Locate every Plasmodium falciparum-infected red blood cell.
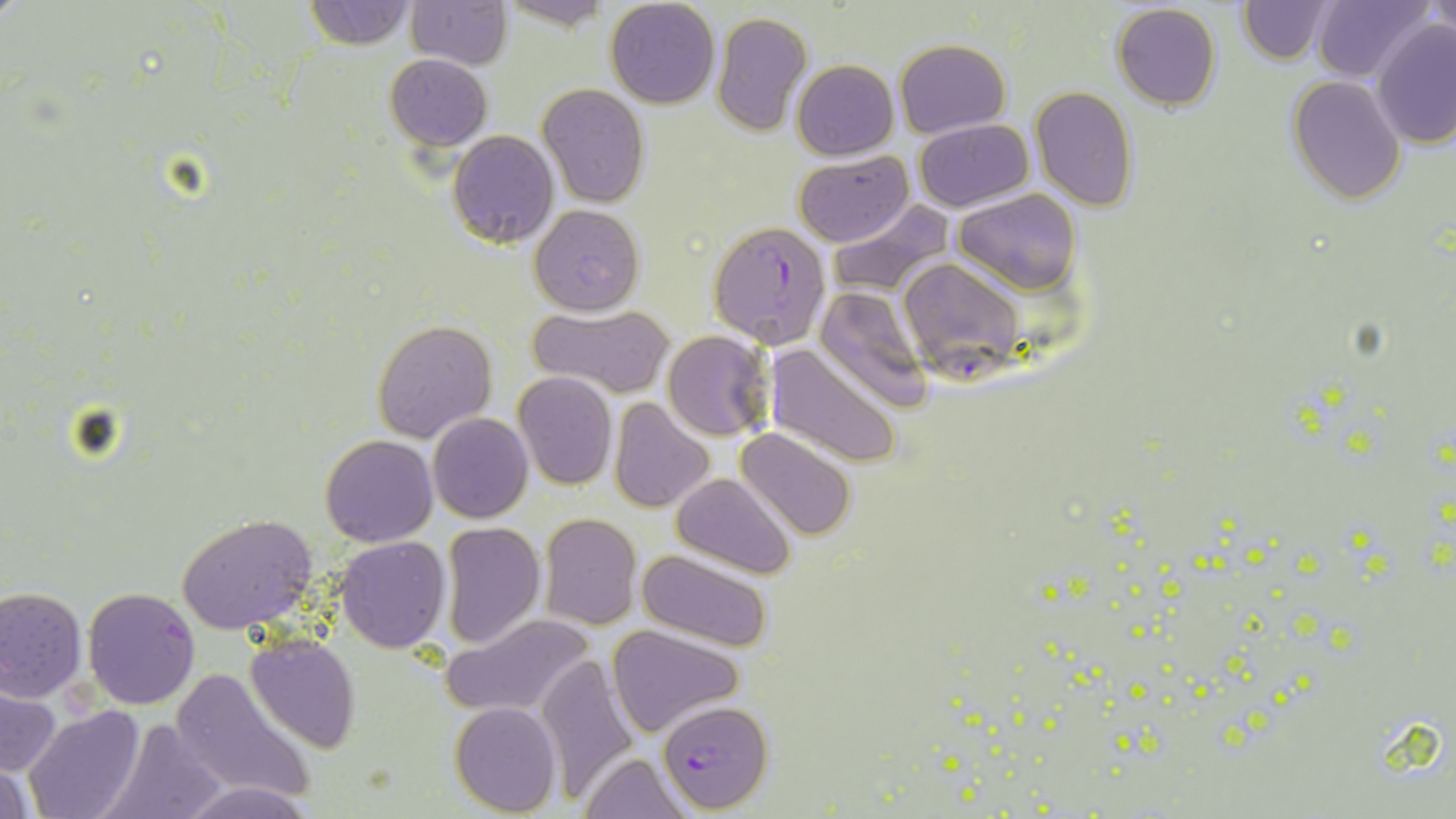
Approximate bounding boxes as [x1, y1, x2, y2] in pixels.
Plasmodium falciparum-infected red blood cells: [707, 220, 834, 349], [897, 257, 1028, 381], [658, 698, 771, 811].

slide-level diagnosis = Plasmodium falciparum
image size = 1456×819 pixels
stain = May-Grünwald-Giemsa
preparation = thin blood smear
field of view = one of a larger specimen
uninfected red blood cell locations = approximate bounding boxes as [x1, y1, x2, y2] in pixels: [304, 0, 415, 48], [406, 0, 512, 68], [606, 0, 719, 109], [1237, 0, 1331, 64], [1425, 0, 1455, 38], [1311, 1, 1430, 82], [494, 3, 617, 32], [1112, 5, 1221, 111], [711, 11, 812, 137], [1371, 19, 1456, 150], [894, 38, 1011, 137], [385, 54, 491, 149], [791, 59, 899, 160], [1288, 75, 1406, 205], [538, 83, 650, 207], [1030, 86, 1139, 212], [913, 120, 1033, 212], [448, 130, 558, 249], [793, 149, 912, 247], [954, 189, 1082, 294], [827, 200, 953, 297], [530, 203, 645, 315], [813, 285, 934, 410], [530, 304, 674, 398], [372, 319, 496, 443], [662, 330, 775, 443], [765, 342, 903, 469], [635, 351, 749, 481], [512, 371, 618, 490], [609, 397, 713, 513], [427, 413, 533, 524], [736, 427, 857, 543], [319, 434, 437, 546], [672, 473, 797, 578], [176, 513, 319, 634], [539, 513, 642, 629], [440, 521, 547, 651], [335, 536, 451, 654], [637, 550, 774, 652], [0, 586, 86, 702], [82, 587, 201, 710], [442, 612, 597, 720], [607, 624, 744, 738], [246, 634, 360, 752], [535, 654, 642, 801], [168, 668, 316, 803], [0, 685, 60, 778], [450, 703, 561, 816], [24, 706, 144, 819], [102, 718, 231, 819], [580, 753, 690, 819], [0, 761, 36, 818], [181, 780, 309, 818]
modality = optical microscopy
magnification = 1000x